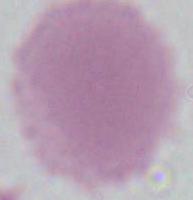
Summary:
  - Modality: micrograph
  - Magnification: 1000x
  - Identification: red blood cell